Identify the parasite.
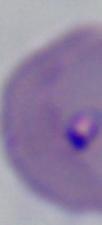
This is Babesia.

Captured at 1000x magnification. Micrograph.